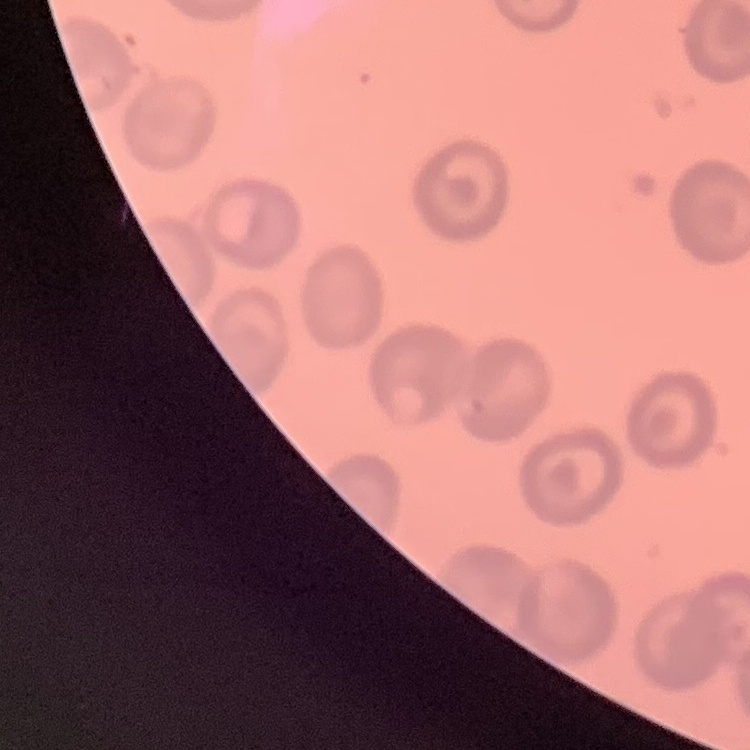
red blood cell morphology = no rouleaux formation
image type = square crop of a larger photomicrograph
preparation = thin blood smear
stain = Field's or Giemsa